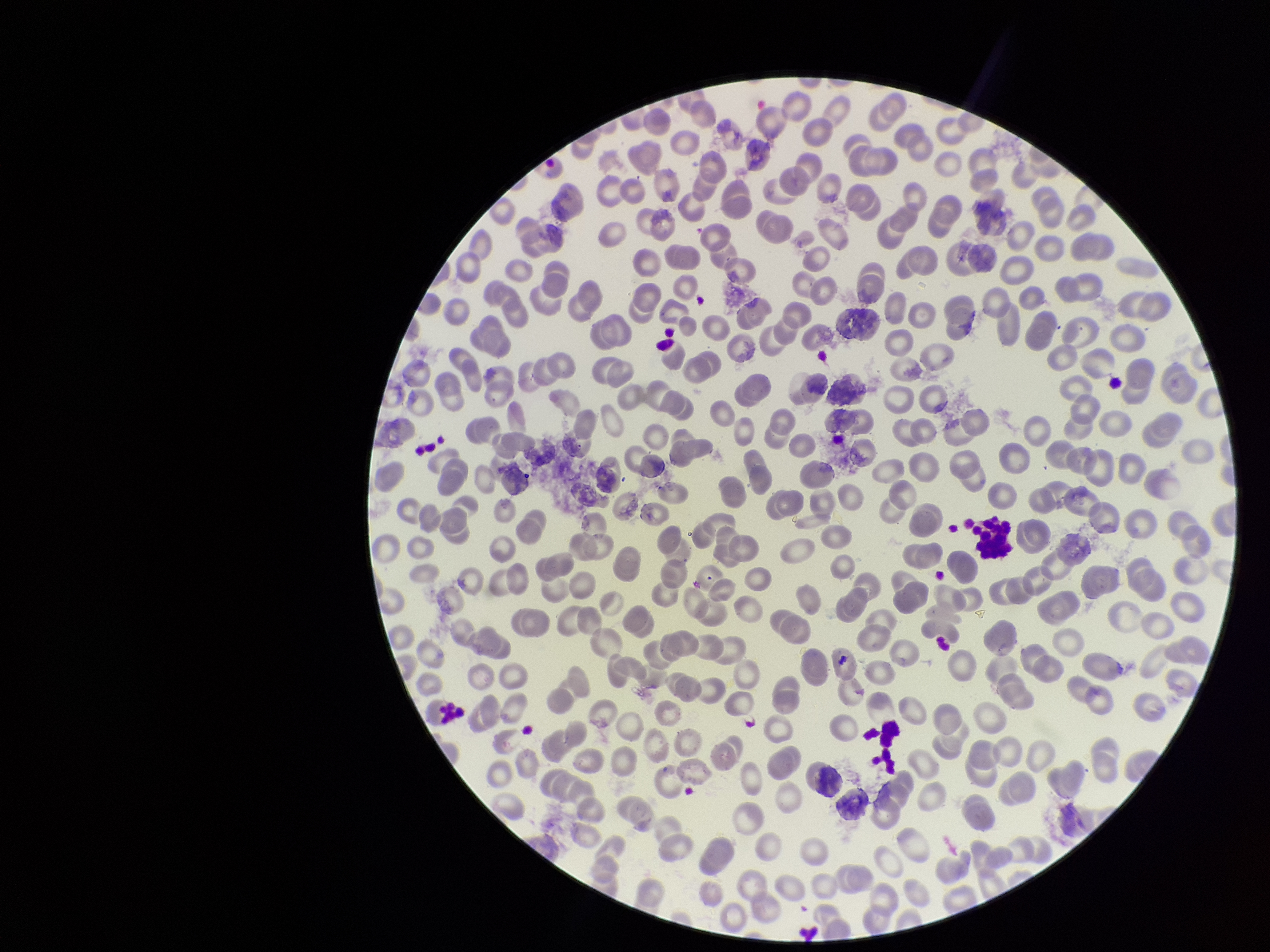

{
  "preparation": "thin blood smear",
  "image_size": "1270×952 pixels",
  "field_of_view": "one from this slide",
  "red_blood_cell_count": 271,
  "parasitized_red_blood_cell_count": 0,
  "stain": "Giemsa",
  "parasitized_red_blood_cells": "none identified",
  "capture": "smartphone photograph through the microscope eyepiece",
  "patient_malaria_status": "negative"
}